Identify the blood parasite species.
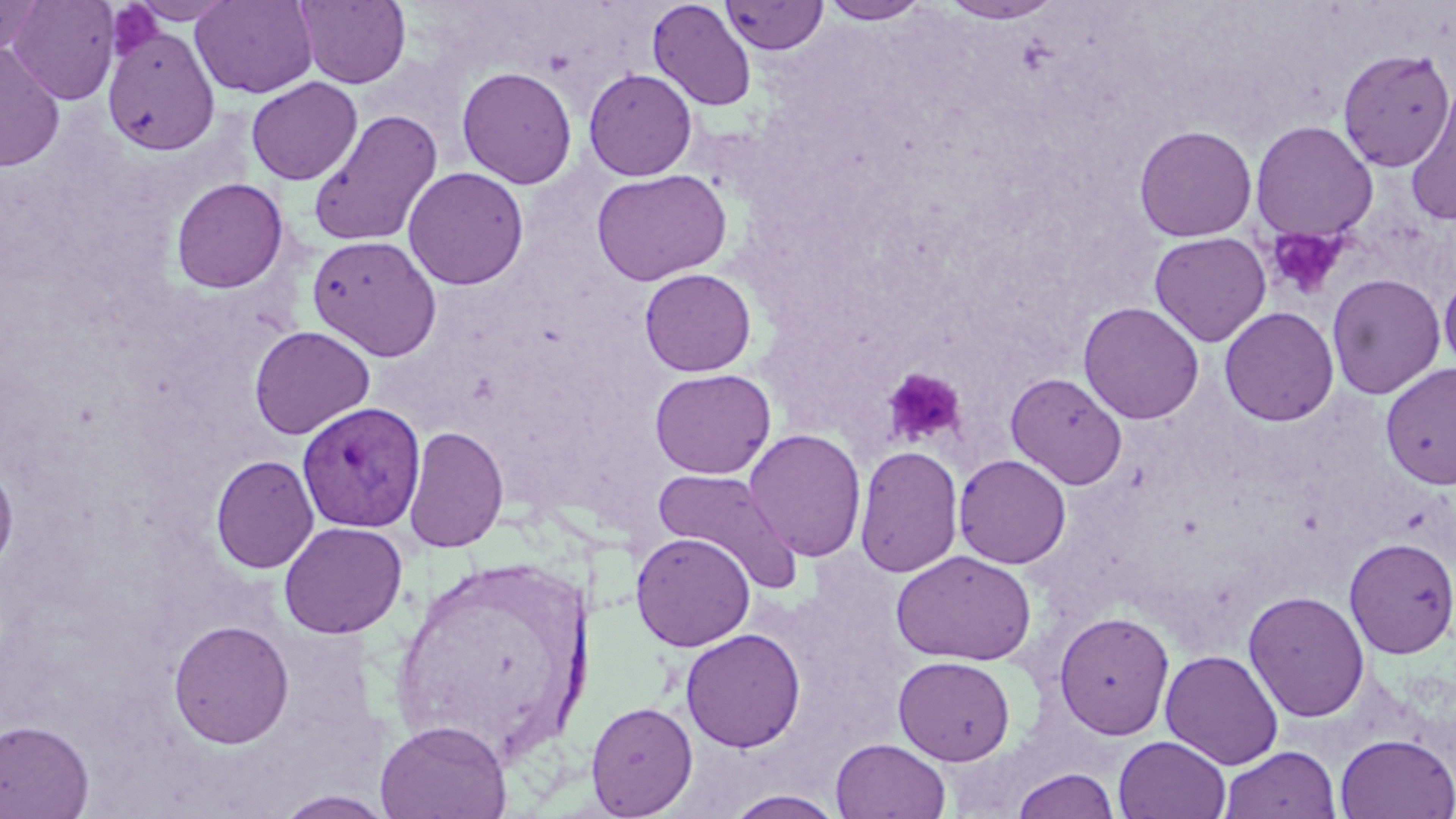
Plasmodium vivax.

{
  "uninfected_red_blood_cell_locations": "approximate bounding boxes as (x1,y1)-(x2,y2) corner pairs in pixels: (0,0)-(44,54), (7,0)-(120,105), (128,0)-(238,24), (191,0)-(317,98), (295,0)-(410,89), (648,0)-(757,112), (721,0)-(828,55), (818,0)-(931,25), (940,0)-(1064,25), (103,26)-(219,155), (0,43)-(65,172), (1336,48)-(1454,172), (457,66)-(577,189), (583,68)-(698,181), (246,77)-(362,185), (1405,82)-(1456,226), (308,108)-(442,247), (1249,120)-(1378,243), (1134,125)-(1258,242), (403,166)-(528,290), (591,168)-(732,286), (170,178)-(290,294), (1149,232)-(1272,346), (307,233)-(443,361), (640,268)-(756,376), (1327,273)-(1446,399), (1439,273)-(1456,376), (1078,301)-(1204,424), (1219,306)-(1339,426), (249,325)-(375,439), (1380,363)-(1456,489), (649,368)-(775,479), (1006,372)-(1127,489), (403,425)-(508,553), (744,428)-(867,562), (855,445)-(963,578), (211,454)-(319,574), (953,454)-(1071,569), (0,456)-(19,576), (652,467)-(802,593), (278,521)-(407,639), (631,532)-(755,652), (1344,537)-(1456,659), (891,549)-(1037,666), (391,561)-(589,754), (1243,590)-(1370,723), (1053,610)-(1175,739), (167,619)-(294,748), (681,627)-(805,752), (1160,649)-(1284,770), (893,655)-(1016,765), (585,701)-(698,817), (375,718)-(512,819), (0,719)-(95,819), (1335,733)-(1456,818), (1114,735)-(1230,819), (831,738)-(951,819), (1220,745)-(1340,819), (1011,768)-(1120,819), (272,790)-(397,818), (725,790)-(846,819)",
  "image_size": "1456×819 pixels",
  "plasmodium_vivax_infected_red_blood_cell_locations": "approximate bounding boxes as (x1,y1)-(x2,y2) corner pairs in pixels: (296,402)-(426,533)",
  "modality": "optical microscopy",
  "magnification": "1000x",
  "preparation": "thin blood smear",
  "platelet_locations": "approximate bounding boxes as (x1,y1)-(x2,y2) corner pairs in pixels: (108,3)-(165,59), (1265,226)-(1347,300), (883,367)-(966,447)",
  "stain": "May-Grünwald-Giemsa",
  "field_of_view": "single"
}